Describe the morphology of the erythrocytes.
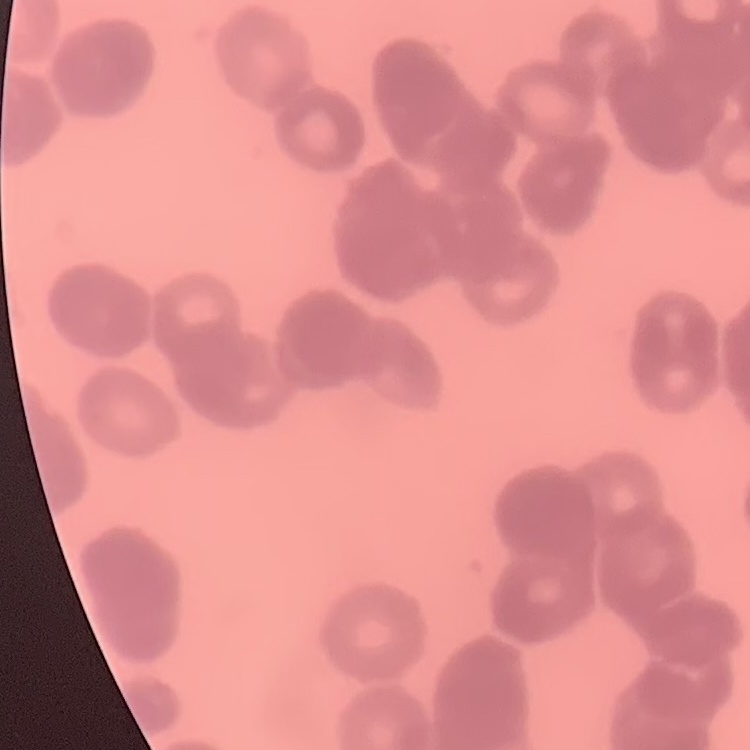

Rouleaux formation.

Summary:
  - Image type: one tile cut from a larger photomicrograph
  - Stain: Field's or Giemsa
  - Preparation: thin blood smear